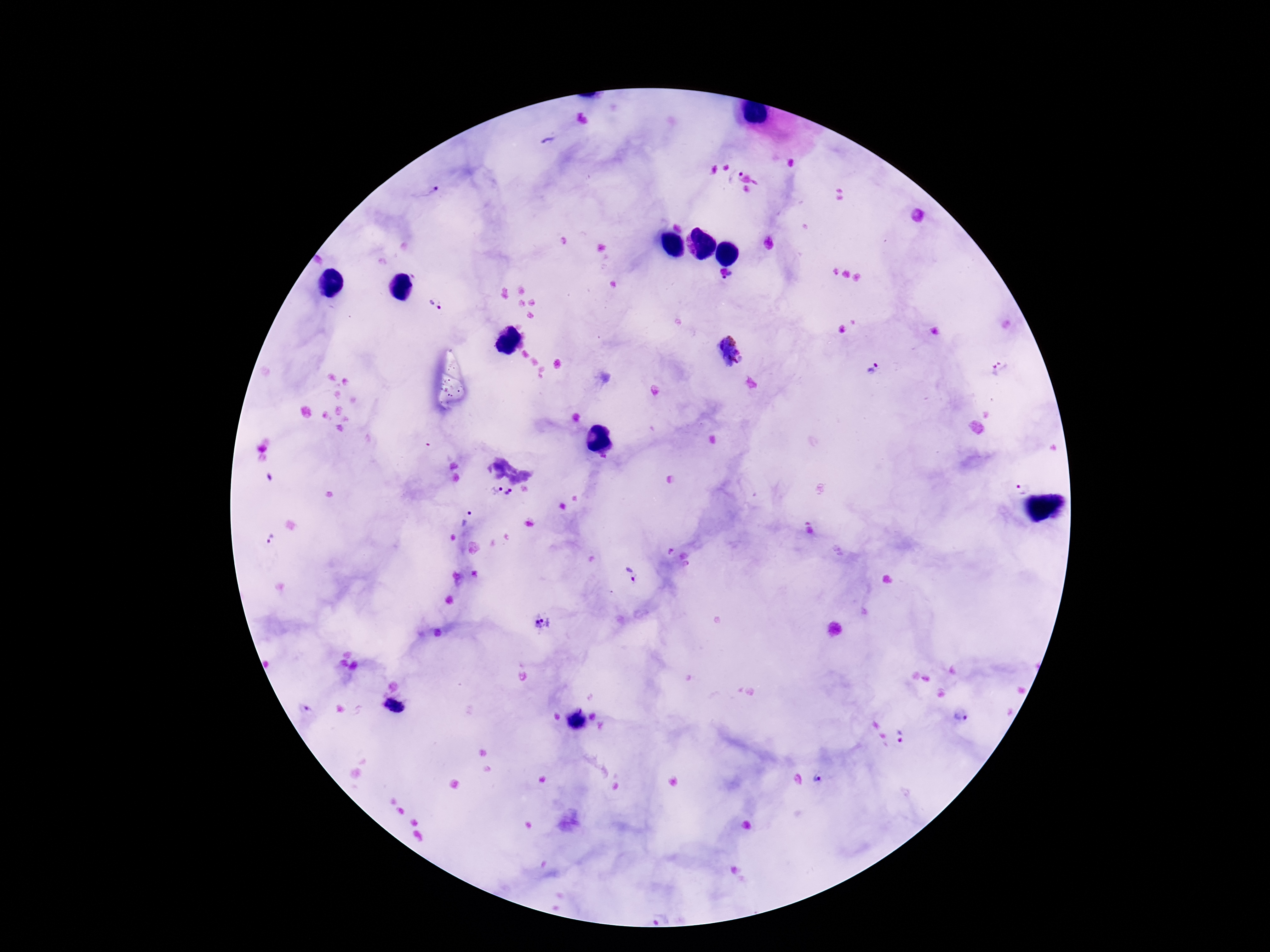 Approximate object centers, in pixels from the top-left corner. Plasmodium parasite locations: (x=547, y=141), (x=734, y=176), (x=428, y=192), (x=729, y=279), (x=437, y=304), (x=729, y=351), (x=871, y=368), (x=1001, y=370), (x=1021, y=488), (x=495, y=490), (x=512, y=494), (x=466, y=519), (x=272, y=538), (x=632, y=576), (x=545, y=623), (x=396, y=707), (x=961, y=714), (x=902, y=735), (x=818, y=779). Single field of view. Patient malaria status: positive. Giemsa stain. Thick blood smear. Photographed through the microscope eyepiece with a smartphone camera. 100x magnification. Image is 1270×952 pixels.